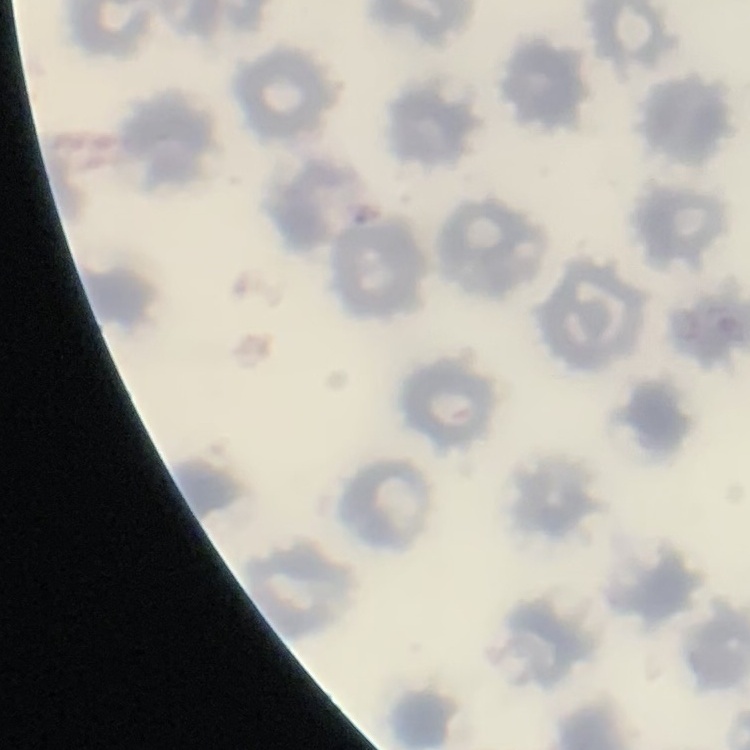
red blood cell morphology = no rouleaux formation
preparation = thin blood film
image type = one tile cut from a larger photomicrograph
stain = Field's or Giemsa